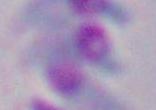
Summary:
  - Modality: micrograph
  - Magnification: 1000x
  - Identification: Toxoplasma gondii